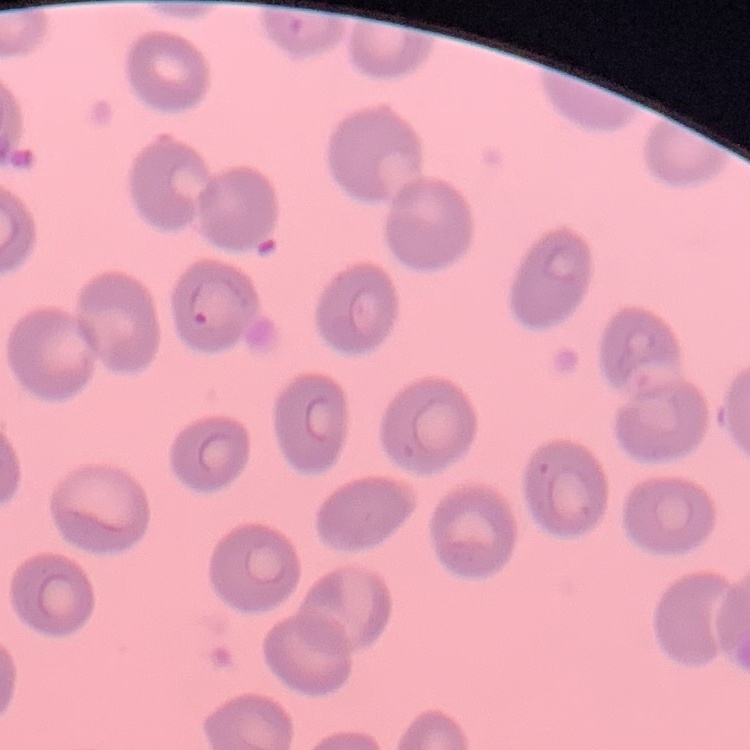
The erythrocytes exhibit no rouleaux formation. Square crop of a larger photomicrograph. Thin peripheral smear. Stained with either Field's or Giemsa.